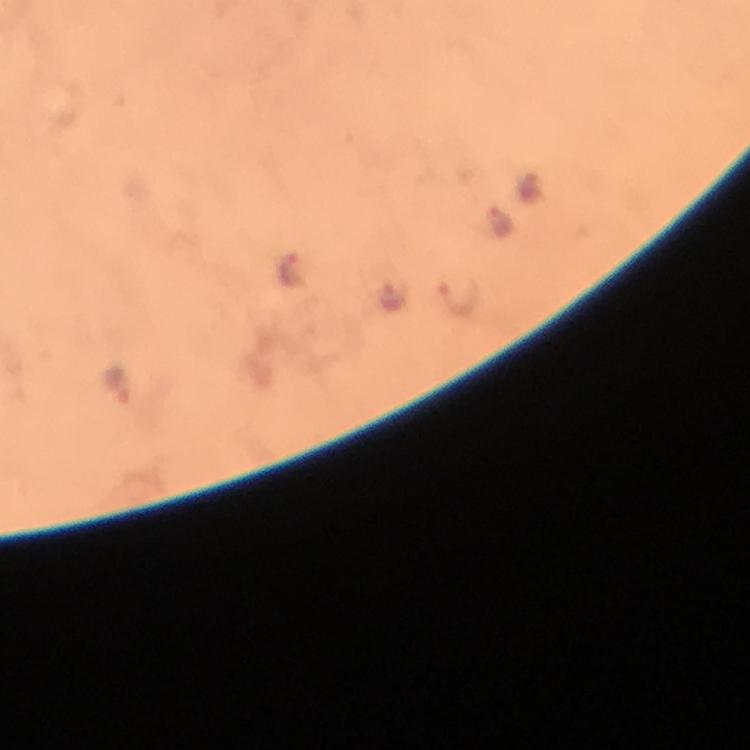

Approximate centers as {x, y} in pixels. Plasmodium parasite locations: {500, 221}, {290, 268}, {458, 296}, {392, 297}, {118, 383}. Thick blood film. Cropped region of a single field of view. From a malaria diagnostic workup. Image is 750×750 pixels. Photographed through the microscope with a smartphone camera. At 100x magnification. Giemsa stain. Immersion oil applied.